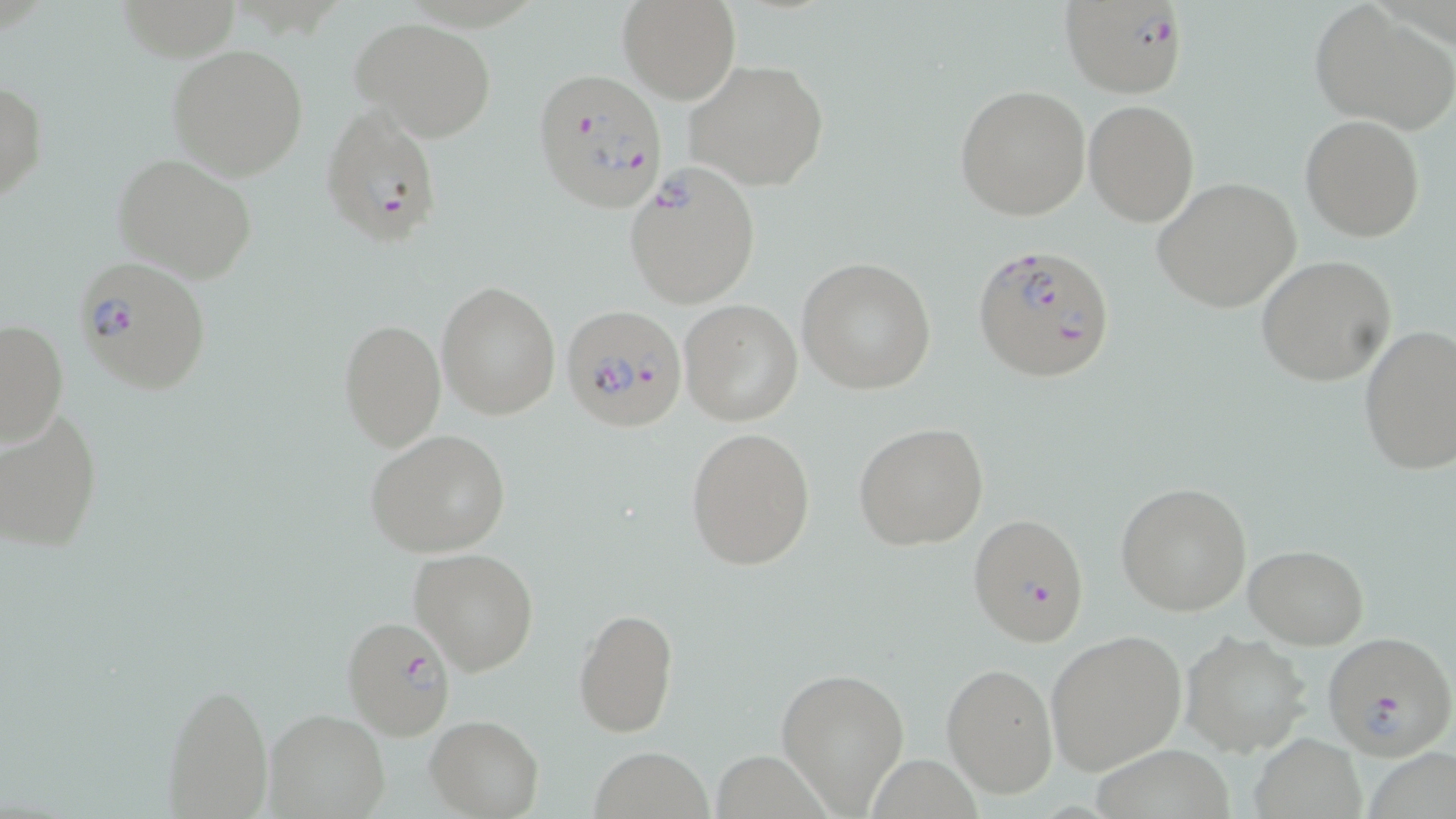
Approximate bounding boxes as [x1, y1, x2, y2] in pixels. Plasmodium falciparum-infected red blood cell locations: [1059, 1, 1189, 98], [531, 65, 667, 213], [321, 105, 445, 249], [624, 164, 761, 310], [971, 241, 1116, 382], [71, 255, 212, 397], [561, 302, 688, 433], [967, 513, 1089, 647], [340, 616, 458, 742], [1321, 631, 1455, 759]. Uninfected red blood cell locations: [617, 0, 741, 106], [1309, 2, 1456, 134], [350, 17, 496, 140], [166, 42, 309, 180], [685, 59, 829, 192], [1, 80, 48, 203], [954, 84, 1090, 221], [1083, 101, 1197, 225], [1300, 115, 1426, 242], [113, 152, 260, 284], [1151, 177, 1302, 312], [1255, 255, 1397, 386], [797, 256, 936, 394], [437, 280, 561, 420], [679, 301, 802, 426], [0, 319, 68, 448], [337, 319, 445, 451], [1357, 324, 1456, 476], [0, 404, 104, 553], [852, 421, 989, 551], [686, 427, 816, 570], [365, 428, 511, 558], [1116, 481, 1254, 616], [1243, 544, 1369, 648], [409, 548, 539, 675], [574, 608, 678, 736], [1045, 629, 1188, 775], [1181, 633, 1312, 757], [941, 661, 1058, 799], [776, 666, 910, 812], [159, 679, 275, 819], [265, 709, 389, 819], [425, 714, 544, 818], [1252, 732, 1367, 819], [1093, 745, 1235, 818], [588, 746, 714, 818]. Slide-level diagnosis: Plasmodium falciparum. Light microscopy. 1000x magnification. May-Grünwald-Giemsa stain. Image is 1456×819 pixels. Thin blood film. One field of a larger specimen.